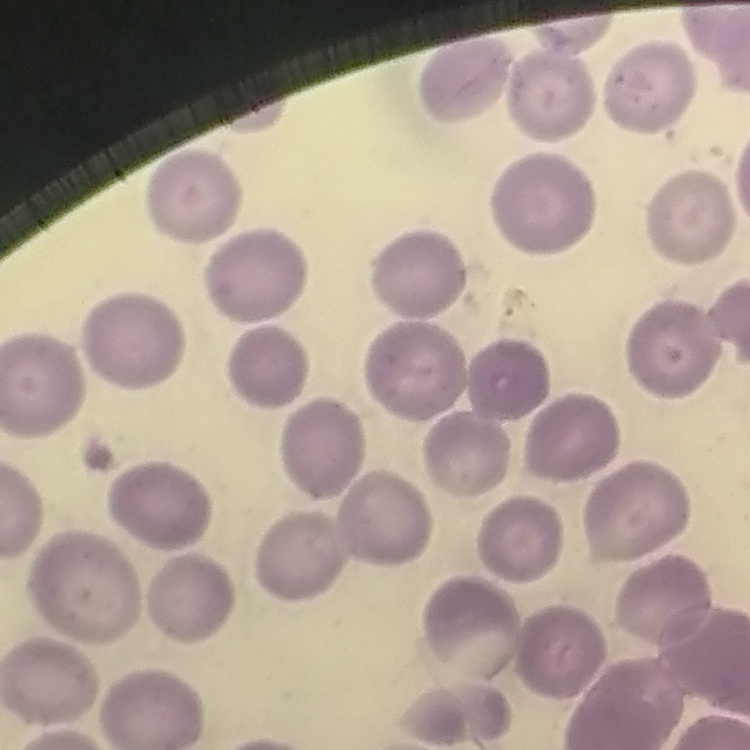
Summary:
  - Erythrocyte morphology: no rouleaux formation
  - Preparation: thin blood smear
  - Stain: Field's or Giemsa
  - Image type: one tile cut from a larger photomicrograph